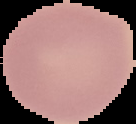 Image is 136×124 pixels. Malaria status: uninfected. From a thin blood smear. The area outside the segmented cell region is set to black.